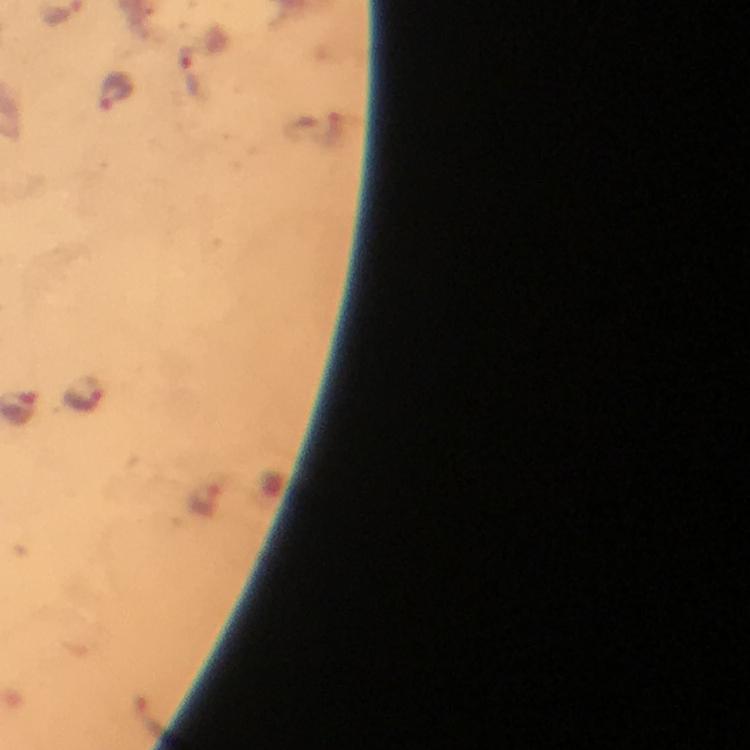
{
  "context": "from a diagnostic examination for malaria",
  "preparation": "thick blood film",
  "cropped_from": "a single field of view",
  "immersion_oil": "applied",
  "plasmodium_parasite_locations": "approximate centers as [x, y] in pixels: [189, 69], [114, 92], [83, 394]",
  "image_size": "750×750 pixels",
  "magnification": "100x",
  "capture": "smartphone camera through the microscope",
  "stain": "Giemsa"
}